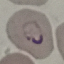

malaria_status: parasitized
preparation: thin smear
image_type: cell patch, automatically extracted from a larger field of view and resized to 64 × 64 pixels
stain: Giemsa
capture: smartphone camera at the microscope eyepiece